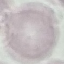
malaria status = uninfected
capture = smartphone through the microscope eyepiece
image type = cell patch, automatically extracted from a larger field of view and resized to 64 × 64 pixels
stain = Giemsa
preparation = thin blood smear